Give the position of every Plasmodium parasite visible.
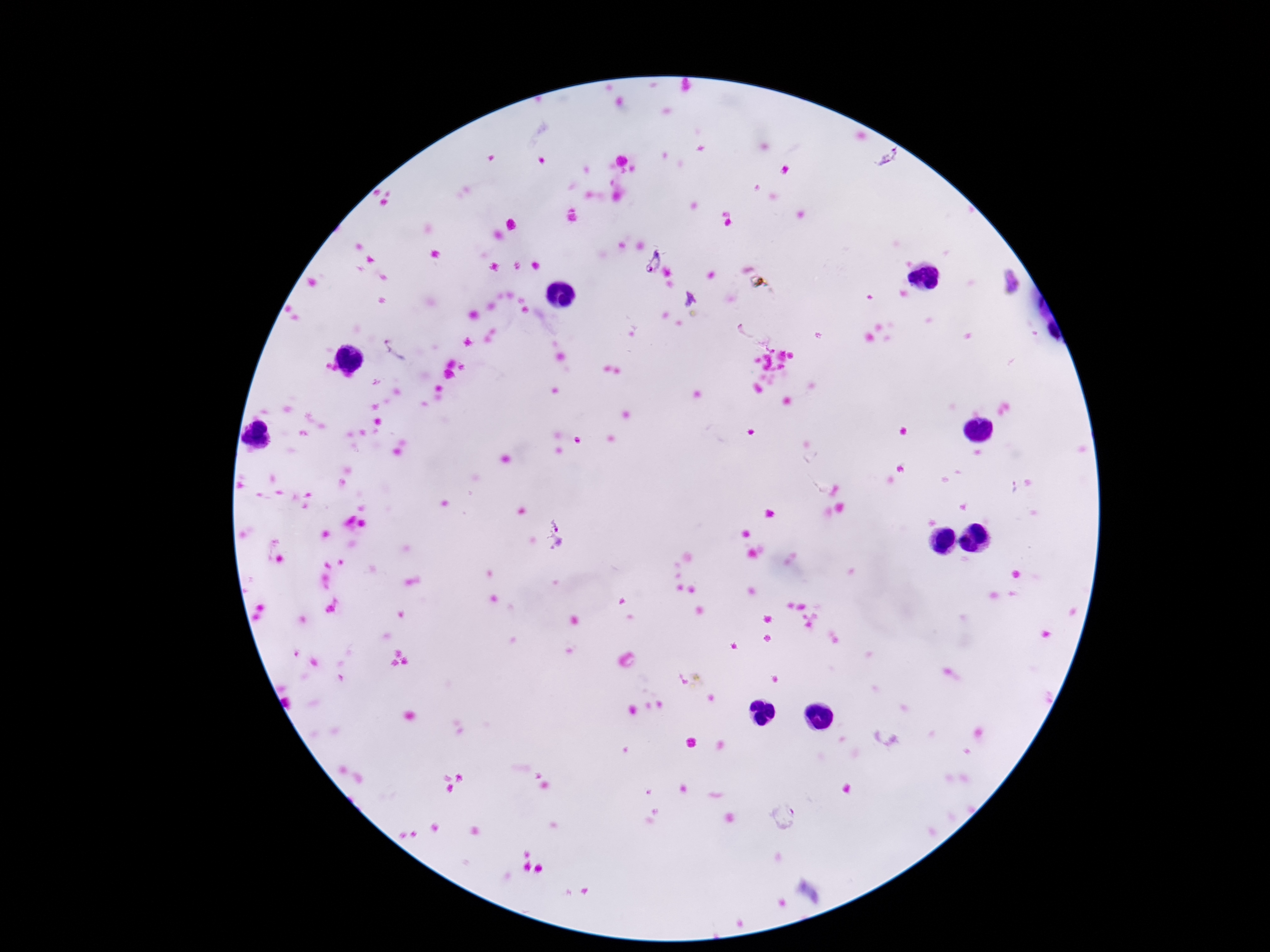
Approximate centers as (x, y) in pixels.
Plasmodium parasites: (888, 158), (651, 261), (1013, 283), (688, 298), (397, 348), (560, 536), (785, 817).

Patient malaria status: infected. 100x magnification. Single field of view. Thick peripheral-blood smear. Giemsa stain. Smartphone photograph taken through the microscope eyepiece. Image is 1270×952 pixels.